Locate every leukocyte (white blood cell).
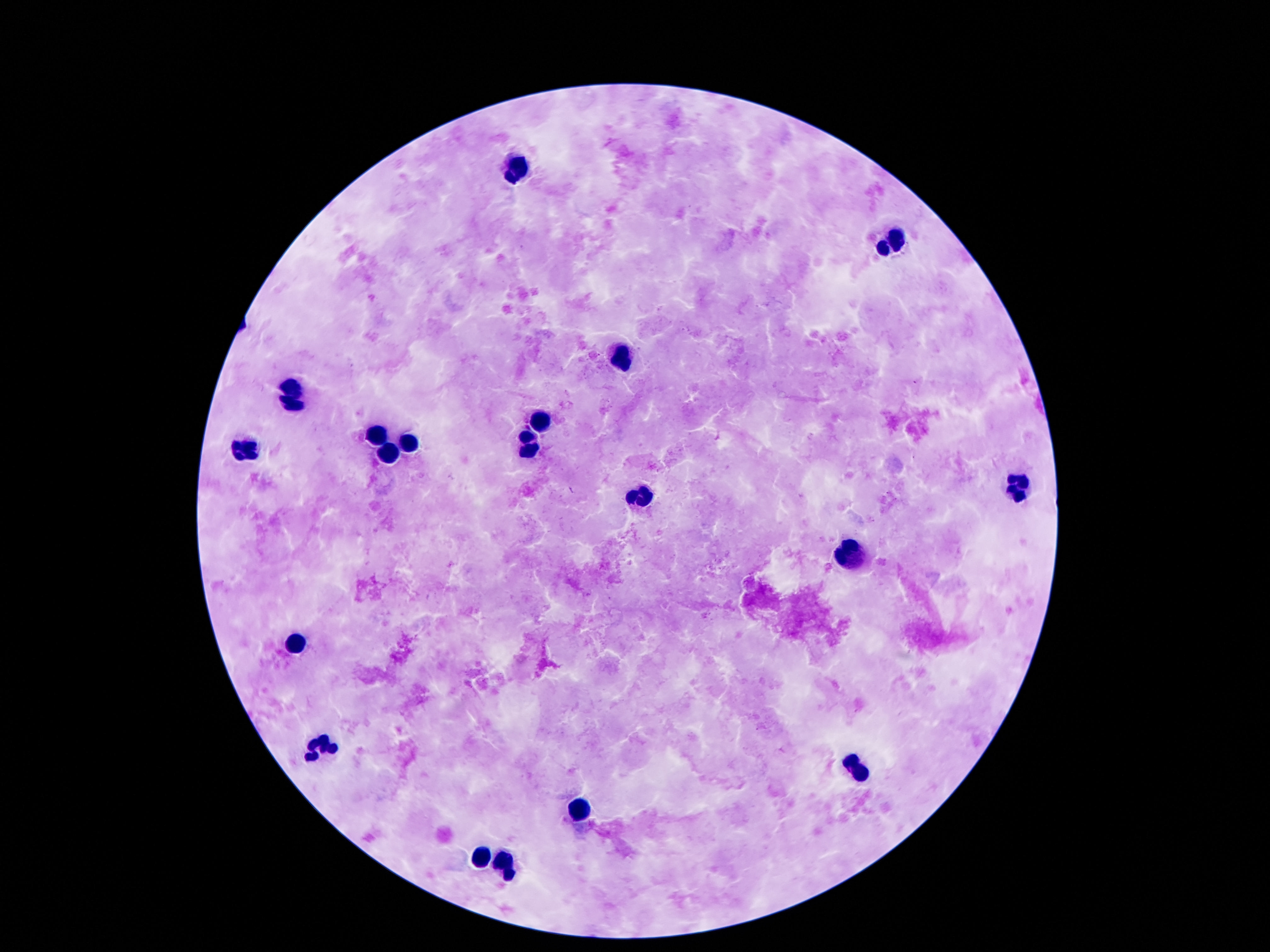
Approximate object centers, in pixels from the top-left corner.
Leukocytes: (x=516, y=169), (x=891, y=238), (x=619, y=356), (x=291, y=394), (x=539, y=419), (x=373, y=436), (x=407, y=446), (x=249, y=448), (x=530, y=448), (x=388, y=452), (x=1017, y=486), (x=640, y=497), (x=849, y=557), (x=293, y=645), (x=320, y=747), (x=858, y=770), (x=577, y=814), (x=478, y=858), (x=507, y=875).

{
  "capture": "smartphone camera through the microscope eyepiece",
  "stain": "Giemsa",
  "magnification": "100x",
  "field_of_view": "one from this slide",
  "image_size": "1270×952 pixels",
  "patient_malaria_status": "uninfected",
  "preparation": "thick blood film"
}